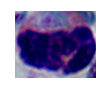

magnification: 1000x
identification: leukocyte
modality: micrograph